Identify the cell.
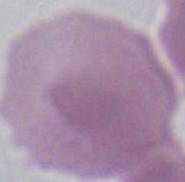
This is an erythrocyte.

magnification = 1000x
modality = micrograph